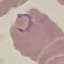
Summary:
  - Malaria status: parasitized
  - Image type: automatically extracted cell patch, resized to 64 × 64 pixels
  - Preparation: thin smear
  - Stain: Giemsa
  - Capture: smartphone camera at the microscope eyepiece